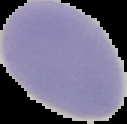
Cell region segmented out of the field of view; the surrounding area is masked to black. From a thin blood smear. Malaria status: uninfected. Image is 127×124 pixels.